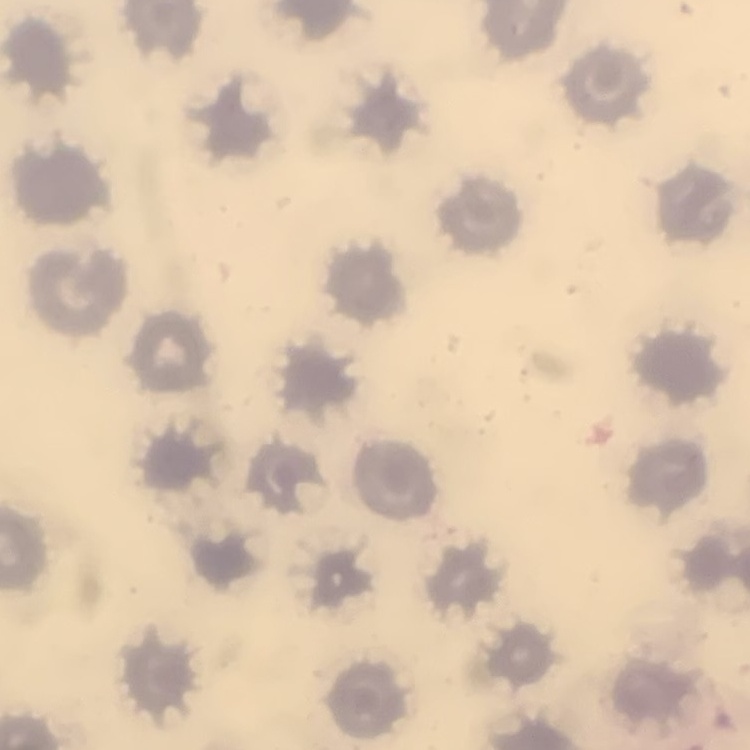
Summary:
  - Erythrocyte morphology: no rouleaux formation
  - Preparation: thin blood smear
  - Stain: Field's or Giemsa
  - Image type: square crop of a larger photomicrograph